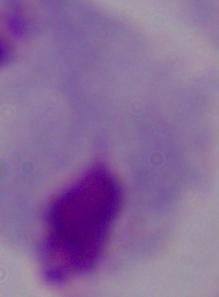
magnification: 1000x
identification: trichomonad
modality: micrograph